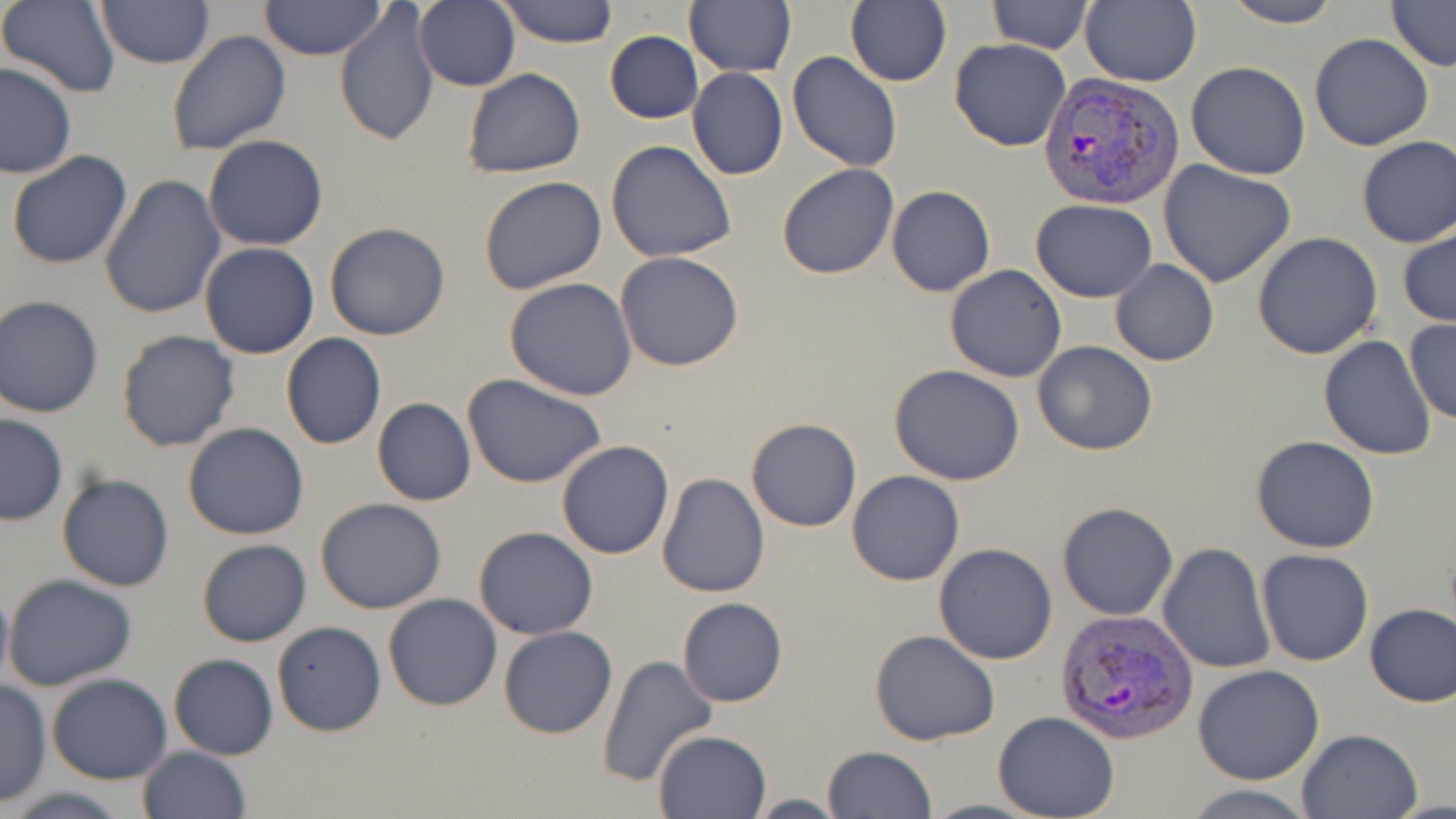

slide-level diagnosis = Plasmodium vivax
modality = optical microscopy
uninfected red blood cell locations = approximate bounding boxes as (x1, y1, x2, y2) in pixels: (413, 0, 521, 93), (496, 0, 619, 48), (845, 0, 951, 88), (986, 0, 1093, 53), (1080, 0, 1200, 86), (1220, 0, 1344, 28), (1385, 0, 1456, 70), (2, 1, 121, 98), (259, 1, 385, 62), (94, 2, 216, 69), (335, 2, 440, 147), (685, 2, 795, 77), (166, 30, 292, 156), (605, 31, 702, 124), (1310, 34, 1435, 151), (949, 37, 1072, 152), (787, 51, 902, 172), (0, 62, 76, 179), (1185, 62, 1311, 181), (461, 68, 585, 179), (688, 68, 788, 181), (203, 135, 328, 252), (1355, 136, 1456, 248), (605, 140, 736, 263), (6, 151, 133, 270), (1157, 160, 1297, 288), (775, 165, 898, 280), (100, 174, 225, 320), (477, 176, 609, 296), (886, 185, 996, 297), (1032, 199, 1158, 302), (1397, 222, 1456, 330), (324, 223, 450, 341), (1251, 232, 1383, 359), (199, 241, 319, 358), (614, 251, 745, 371), (1111, 259, 1218, 366), (945, 264, 1067, 383), (504, 277, 637, 401), (0, 295, 105, 419), (1403, 320, 1456, 424), (116, 329, 240, 451), (281, 333, 386, 451), (1319, 335, 1436, 460), (1033, 341, 1158, 456), (888, 365, 1025, 484), (462, 374, 608, 491), (371, 397, 475, 506), (0, 414, 68, 525), (745, 419, 861, 533), (183, 422, 309, 540), (1250, 437, 1381, 553), (556, 440, 674, 559), (846, 470, 965, 586), (57, 472, 175, 591), (657, 473, 769, 599), (316, 498, 447, 613), (1057, 501, 1179, 621), (473, 526, 597, 640), (196, 538, 313, 646), (1156, 542, 1275, 673), (934, 543, 1057, 664), (1256, 548, 1374, 666), (3, 572, 139, 694), (0, 582, 13, 693), (384, 593, 501, 711), (678, 598, 787, 707), (1364, 602, 1456, 708), (273, 621, 386, 737), (497, 626, 617, 739), (869, 630, 1000, 746), (168, 652, 278, 761), (595, 653, 718, 787), (1193, 666, 1324, 785), (47, 673, 173, 785), (0, 681, 51, 807), (992, 712, 1120, 819), (1296, 728, 1423, 819), (652, 729, 770, 818), (823, 745, 937, 819), (135, 746, 251, 819), (1181, 784, 1319, 819), (6, 787, 132, 819), (746, 794, 845, 818)
Plasmodium vivax-infected red blood cell locations = approximate bounding boxes as (x1, y1, x2, y2) in pixels: (1038, 74, 1184, 211), (1055, 607, 1197, 744)
image size = 1456×819 pixels
preparation = thin blood film
field of view = single
magnification = 1000x
stain = May-Grünwald-Giemsa